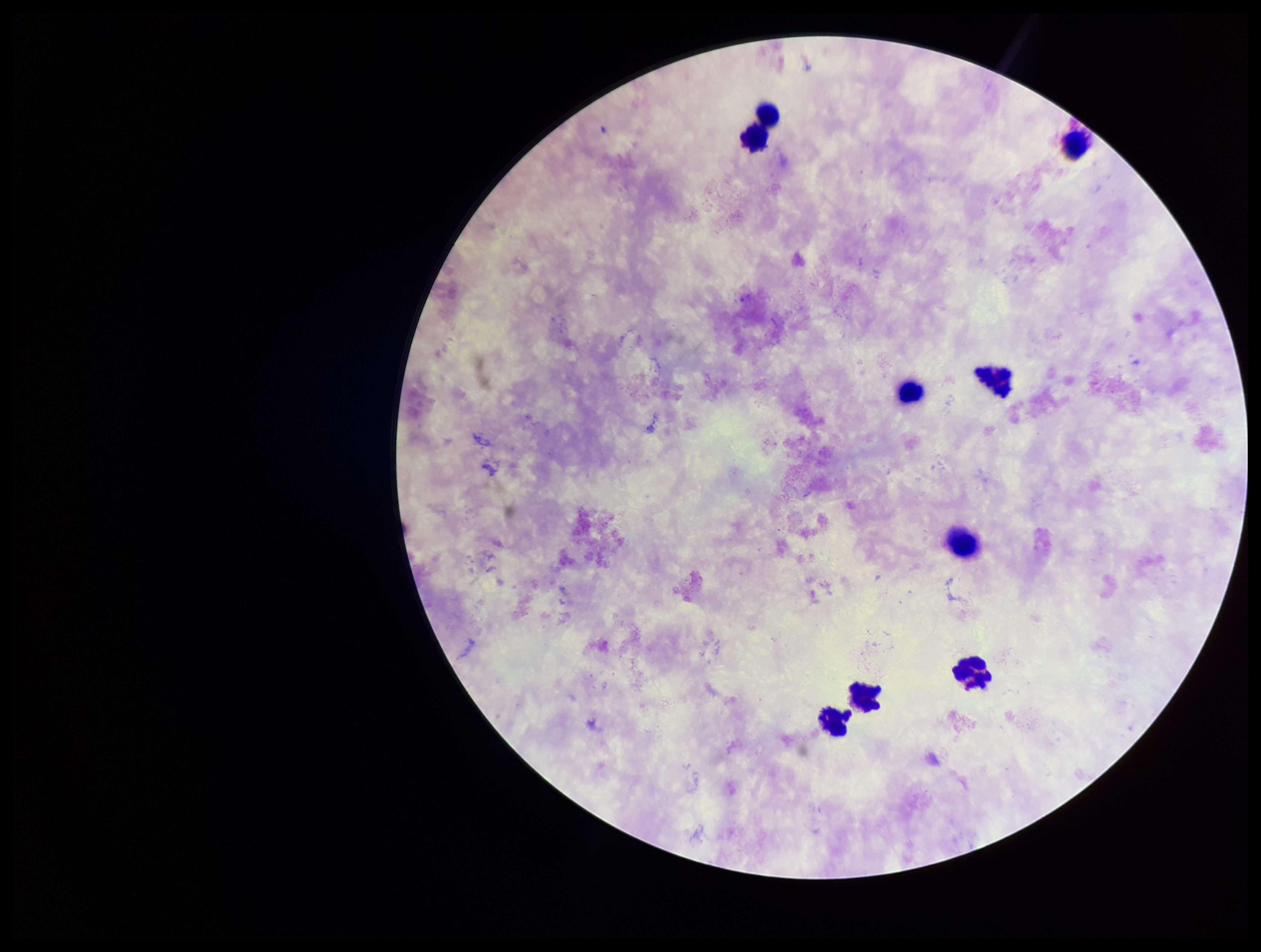
Summary:
  - Preparation: thick blood smear
  - Image size: 1261×952 pixels
  - Patient malaria status: negative
  - Plasmodium parasites: none identified
  - Stain: Giemsa
  - Leukocyte count: 9
  - Capture: smartphone photograph through the microscope eyepiece
  - Parasite count: 0
  - Field of view: one from this slide